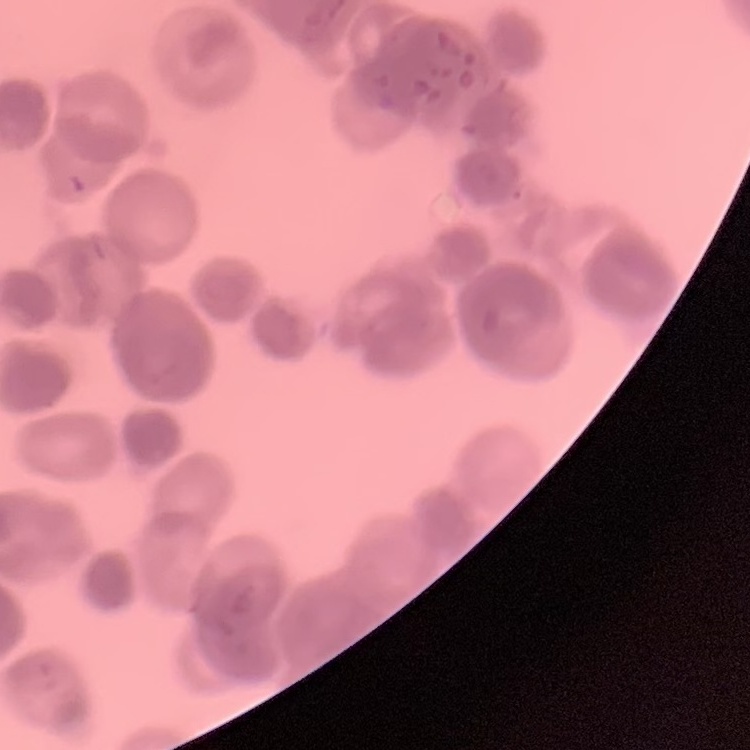
Summary:
  - Erythrocyte morphology: rouleaux formation
  - Image type: square crop of a larger photomicrograph
  - Stain: Field's or Giemsa
  - Preparation: thin blood smear